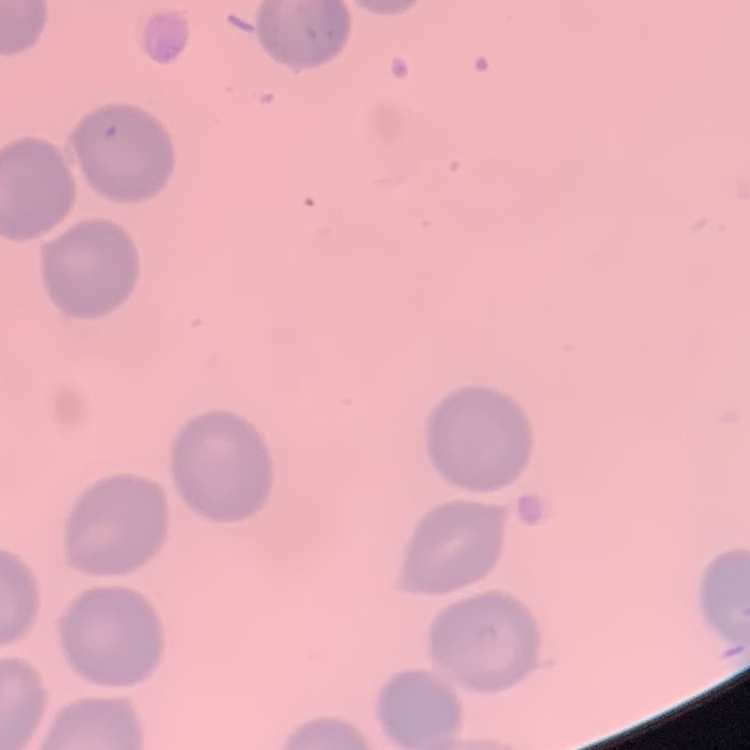

Summary:
  - Red blood cell morphology: no rouleaux formation
  - Image type: one tile cut from a larger photomicrograph
  - Stain: Field's or Giemsa
  - Preparation: thin blood film